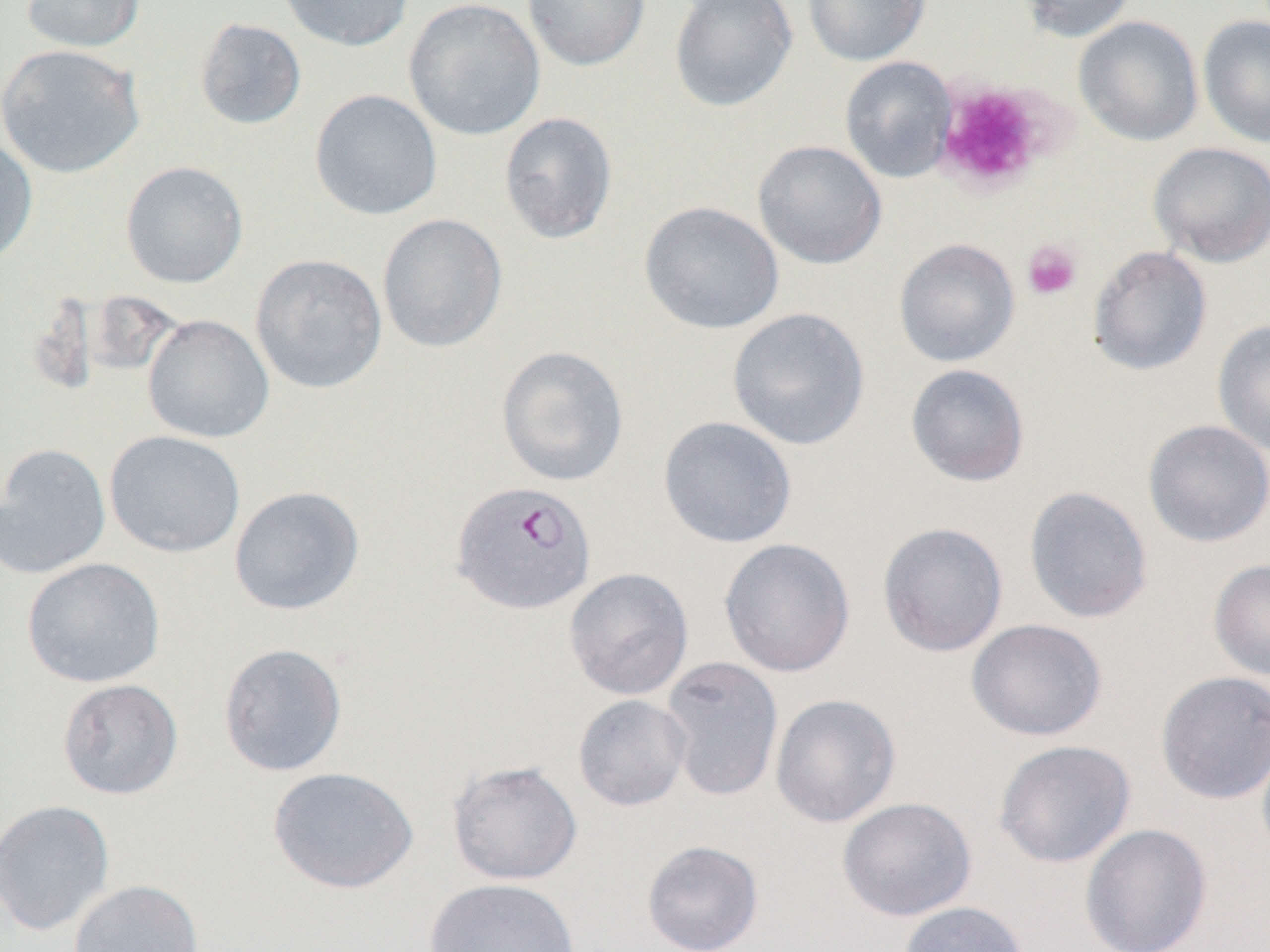
{
  "slide_level_diagnosis": "Plasmodium falciparum",
  "modality": "optical microscopy",
  "magnification": "1000x",
  "image_size": "1270×952 pixels",
  "preparation": "thin blood film",
  "field_of_view": "single",
  "plasmodium_falciparum_infected_red_blood_cell_locations": "approximate bounding boxes as named x1/y1/x2/y2 corners in pixels: (x1=450, y1=481, x2=596, y2=615)",
  "uninfected_red_blood_cell_locations": "approximate bounding boxes as named x1/y1/x2/y2 corners in pixels: (x1=21, y1=0, x2=145, y2=53), (x1=276, y1=0, x2=415, y2=52), (x1=403, y1=0, x2=546, y2=141), (x1=522, y1=0, x2=650, y2=71), (x1=669, y1=0, x2=798, y2=113), (x1=802, y1=0, x2=931, y2=66), (x1=1015, y1=0, x2=1138, y2=42), (x1=1197, y1=13, x2=1270, y2=149), (x1=1073, y1=15, x2=1204, y2=147), (x1=194, y1=18, x2=307, y2=130), (x1=0, y1=44, x2=146, y2=178), (x1=839, y1=56, x2=958, y2=183), (x1=309, y1=89, x2=443, y2=221), (x1=498, y1=111, x2=618, y2=244), (x1=0, y1=133, x2=38, y2=266), (x1=753, y1=139, x2=887, y2=269), (x1=1149, y1=142, x2=1270, y2=267), (x1=120, y1=160, x2=249, y2=288), (x1=639, y1=201, x2=785, y2=334), (x1=377, y1=213, x2=508, y2=353), (x1=893, y1=238, x2=1021, y2=367), (x1=1088, y1=245, x2=1212, y2=377), (x1=250, y1=254, x2=388, y2=394), (x1=726, y1=307, x2=871, y2=451), (x1=142, y1=314, x2=275, y2=443), (x1=1212, y1=319, x2=1270, y2=456), (x1=495, y1=345, x2=629, y2=487), (x1=905, y1=363, x2=1030, y2=487), (x1=657, y1=416, x2=797, y2=548), (x1=1142, y1=419, x2=1270, y2=548), (x1=104, y1=430, x2=246, y2=558), (x1=0, y1=443, x2=111, y2=578), (x1=228, y1=485, x2=365, y2=616), (x1=1024, y1=486, x2=1153, y2=624), (x1=877, y1=521, x2=1009, y2=657), (x1=719, y1=537, x2=856, y2=677), (x1=21, y1=557, x2=165, y2=688), (x1=1208, y1=559, x2=1270, y2=680), (x1=564, y1=567, x2=694, y2=700), (x1=966, y1=618, x2=1108, y2=742), (x1=218, y1=642, x2=348, y2=777), (x1=660, y1=657, x2=784, y2=802), (x1=1155, y1=670, x2=1270, y2=804), (x1=57, y1=678, x2=183, y2=800), (x1=770, y1=693, x2=901, y2=828), (x1=573, y1=694, x2=692, y2=811), (x1=1256, y1=736, x2=1270, y2=864), (x1=993, y1=739, x2=1137, y2=869), (x1=447, y1=760, x2=583, y2=886), (x1=267, y1=766, x2=419, y2=894), (x1=837, y1=796, x2=978, y2=921), (x1=0, y1=799, x2=116, y2=937), (x1=1079, y1=823, x2=1213, y2=952), (x1=641, y1=840, x2=764, y2=952), (x1=423, y1=877, x2=582, y2=952), (x1=68, y1=879, x2=204, y2=952), (x1=899, y1=901, x2=1030, y2=952)",
  "platelet_locations": "approximate bounding boxes as named x1/y1/x2/y2 corners in pixels: (x1=933, y1=80, x2=1054, y2=193), (x1=1022, y1=239, x2=1082, y2=300)"
}